Locate every uninfected red blood cell.
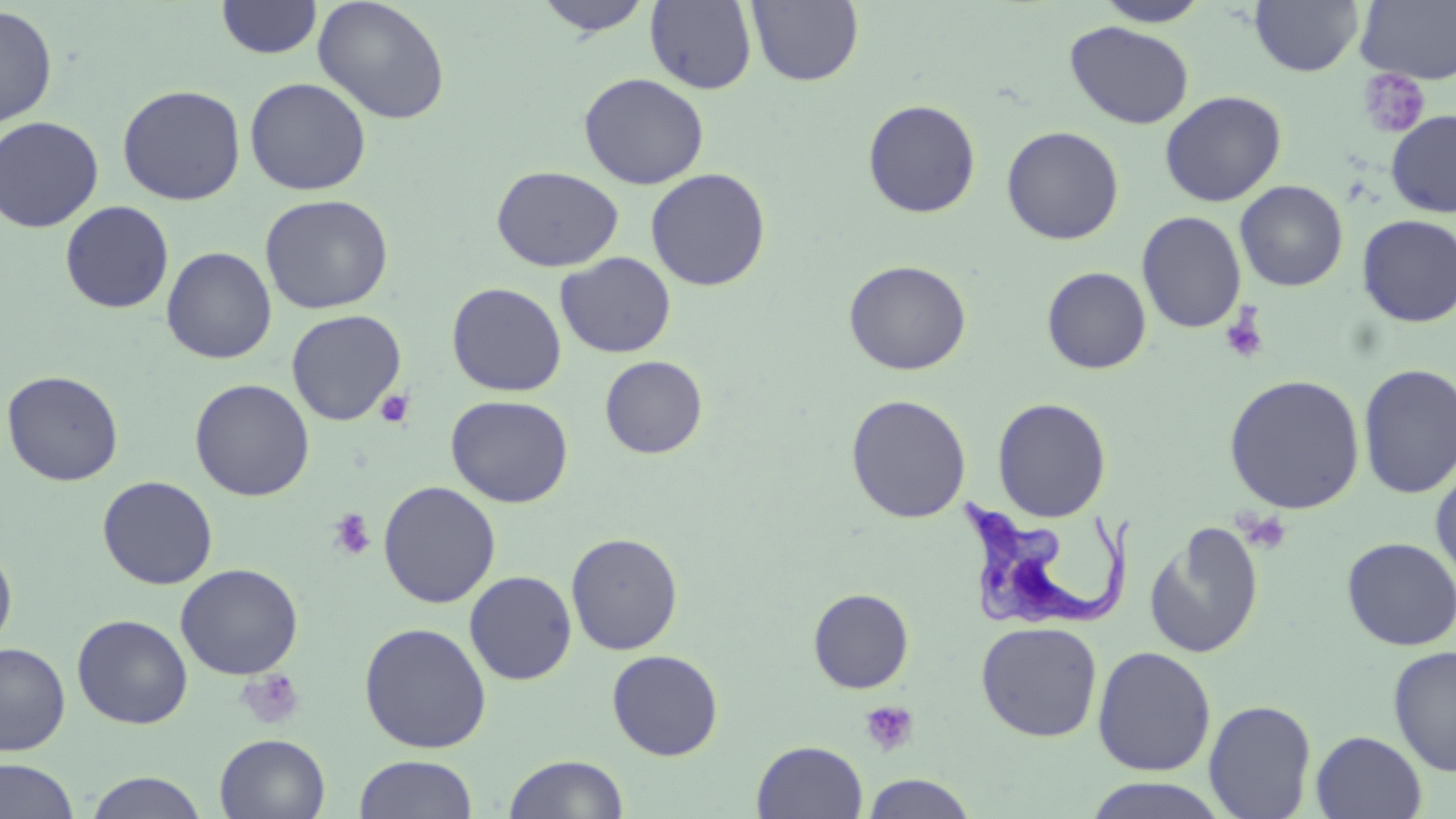

Approximate bounding boxes as (x1, y1, x2, y2) in pixels.
Uninfected red blood cells: (217, 0, 322, 60), (312, 0, 451, 125), (533, 0, 654, 37), (747, 0, 864, 86), (1250, 0, 1364, 76), (645, 1, 757, 94), (1094, 1, 1210, 27), (1355, 1, 1456, 84), (0, 5, 58, 128), (1065, 20, 1194, 130), (578, 72, 709, 190), (244, 77, 371, 196), (117, 84, 246, 206), (1159, 90, 1287, 207), (862, 98, 981, 218), (1385, 109, 1456, 218), (0, 115, 104, 233), (1001, 125, 1124, 245), (491, 165, 624, 272), (645, 167, 771, 292), (1234, 180, 1348, 292), (259, 193, 394, 314), (60, 200, 174, 314), (1136, 211, 1247, 334), (1356, 214, 1456, 327), (161, 246, 277, 364), (556, 252, 675, 358), (843, 259, 972, 375), (1041, 266, 1152, 374), (447, 282, 567, 396), (286, 309, 406, 426), (600, 355, 708, 458), (1357, 363, 1456, 499), (2, 369, 123, 486), (1224, 374, 1365, 514), (189, 378, 315, 501), (846, 394, 971, 523), (446, 395, 573, 508), (992, 397, 1111, 522), (1430, 462, 1456, 585), (98, 475, 218, 589), (377, 480, 501, 608), (1145, 521, 1265, 659), (566, 532, 683, 655), (1341, 537, 1456, 650), (0, 541, 17, 654), (175, 563, 303, 680), (464, 570, 577, 685), (808, 588, 914, 693), (72, 614, 193, 729), (358, 621, 492, 753), (976, 621, 1103, 741), (0, 642, 70, 755), (1388, 645, 1456, 777), (1092, 646, 1216, 777), (607, 649, 724, 760), (1203, 699, 1317, 819), (1310, 731, 1427, 818), (215, 733, 330, 819), (751, 740, 868, 819), (503, 754, 628, 819), (353, 755, 478, 819), (1, 759, 80, 819), (84, 771, 210, 818), (860, 774, 978, 818), (1083, 776, 1230, 818).

Platelet locations: (1356, 68, 1431, 139), (1220, 309, 1269, 364), (375, 389, 416, 428), (329, 508, 377, 561), (1237, 511, 1291, 553), (236, 668, 306, 730), (859, 700, 919, 758). Trypanosoma brucei locations: (958, 497, 1133, 628). Slide-level diagnosis: Trypanosoma brucei. May-Grünwald-Giemsa-stained preparation. Optical microscopy. Thin blood smear. Captured at 1000x magnification. One field of a larger specimen. Image is 1456×819 pixels.